Describe the morphology of the red blood cells.
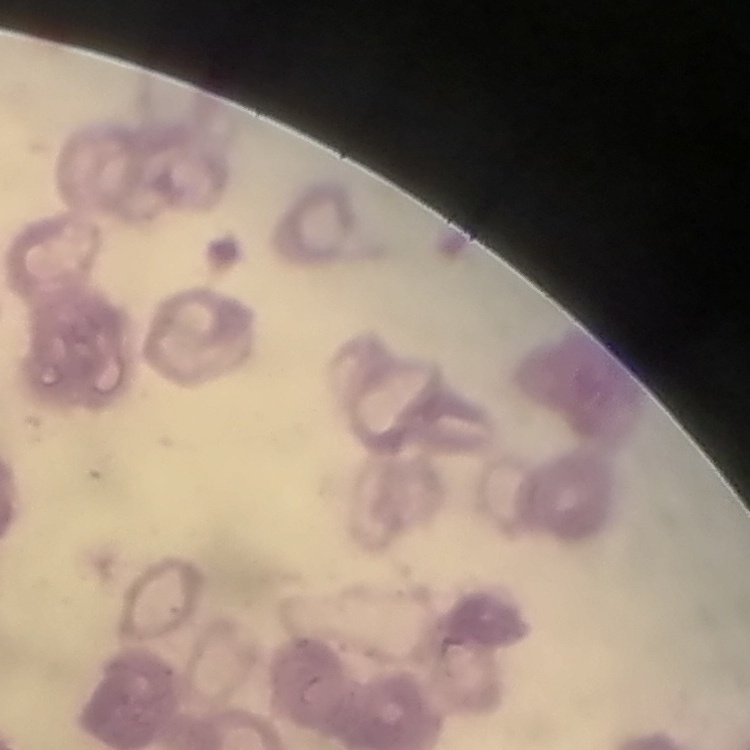
Rouleaux formation.

preparation: thin blood smear
stain: Field's or Giemsa
image_type: square crop of a larger photomicrograph